Locate every blood parasite and identify its species.
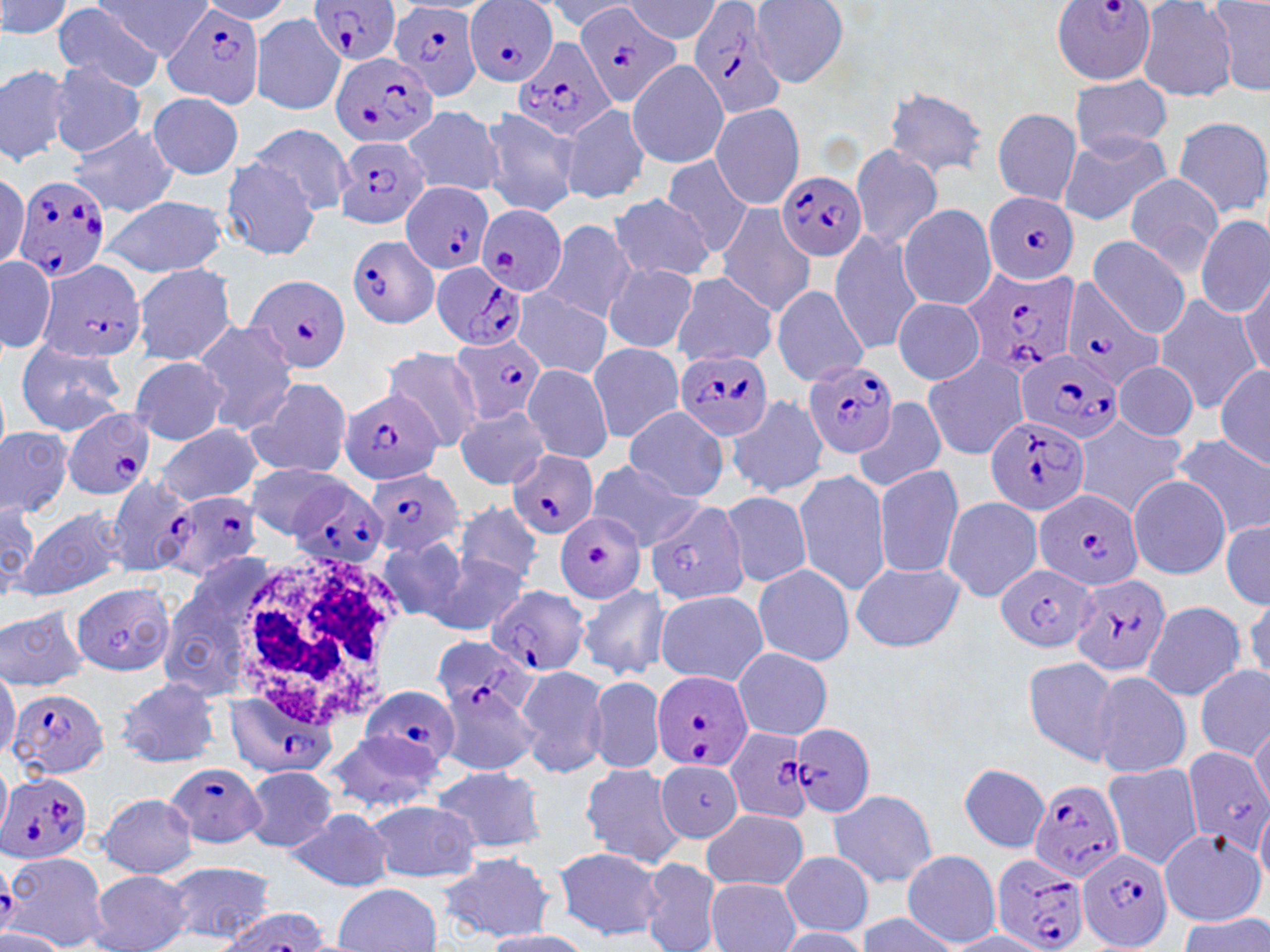
Approximate bounding boxes as named x1/y1/x2/y2 corners in pixels.
Plasmodium falciparum-infected red blood cells (subset): (x1=311, y1=0, x2=402, y2=67), (x1=573, y1=1, x2=683, y2=109), (x1=686, y1=1, x2=788, y2=119), (x1=387, y1=2, x2=485, y2=102), (x1=464, y1=2, x2=560, y2=86), (x1=1051, y1=2, x2=1158, y2=87), (x1=163, y1=4, x2=267, y2=108), (x1=513, y1=36, x2=618, y2=140), (x1=330, y1=50, x2=440, y2=148), (x1=336, y1=135, x2=431, y2=231), (x1=776, y1=171, x2=866, y2=263), (x1=13, y1=175, x2=111, y2=285), (x1=402, y1=181, x2=496, y2=276), (x1=983, y1=191, x2=1079, y2=285), (x1=475, y1=204, x2=567, y2=296), (x1=347, y1=235, x2=439, y2=328), (x1=34, y1=259, x2=147, y2=366), (x1=431, y1=262, x2=530, y2=351), (x1=963, y1=268, x2=1080, y2=379), (x1=243, y1=273, x2=349, y2=375), (x1=1058, y1=280, x2=1165, y2=390), (x1=453, y1=330, x2=546, y2=426), (x1=1015, y1=346, x2=1124, y2=447), (x1=675, y1=347, x2=773, y2=442), (x1=803, y1=358, x2=898, y2=459), (x1=339, y1=385, x2=443, y2=488), (x1=64, y1=408, x2=155, y2=499), (x1=983, y1=414, x2=1091, y2=517), (x1=509, y1=451, x2=597, y2=540), (x1=366, y1=467, x2=468, y2=559), (x1=104, y1=474, x2=193, y2=578), (x1=285, y1=481, x2=389, y2=571), (x1=1033, y1=487, x2=1143, y2=594), (x1=158, y1=492, x2=263, y2=583), (x1=641, y1=500, x2=749, y2=605), (x1=553, y1=514, x2=646, y2=605), (x1=995, y1=563, x2=1098, y2=654), (x1=1070, y1=573, x2=1172, y2=679), (x1=68, y1=581, x2=175, y2=677), (x1=485, y1=586, x2=590, y2=678), (x1=431, y1=638, x2=537, y2=721), (x1=651, y1=669, x2=753, y2=773), (x1=361, y1=686, x2=458, y2=770), (x1=225, y1=688, x2=337, y2=780), (x1=7, y1=689, x2=106, y2=780), (x1=790, y1=724, x2=876, y2=818), (x1=723, y1=727, x2=815, y2=823), (x1=1180, y1=747, x2=1270, y2=854), (x1=166, y1=762, x2=266, y2=848), (x1=0, y1=773, x2=94, y2=866), (x1=1029, y1=780, x2=1127, y2=884), (x1=1077, y1=845, x2=1173, y2=951), (x1=992, y1=850, x2=1090, y2=952).
No Plasmodium ovale, Plasmodium malariae, Plasmodium vivax, Babesia divergens, or Trypanosoma brucei observed.

slide-level diagnosis = Plasmodium falciparum
field of view = one of a larger specimen
modality = light microscopy
white blood cell locations = approximate bounding boxes as named x1/y1/x2/y2 corners in pixels: (x1=234, y1=548, x2=408, y2=725)
image size = 1270×952 pixels
stain = May-Grünwald-Giemsa
magnification = 1000x
preparation = thin blood film
uninfected red blood cell locations (subset) = approximate bounding boxes as named x1/y1/x2/y2 corners in pixels: (x1=0, y1=0, x2=74, y2=43), (x1=99, y1=0, x2=212, y2=59), (x1=197, y1=0, x2=295, y2=23), (x1=1209, y1=0, x2=1270, y2=98), (x1=542, y1=1, x2=638, y2=33), (x1=623, y1=1, x2=722, y2=43), (x1=748, y1=1, x2=851, y2=88), (x1=1136, y1=1, x2=1239, y2=102), (x1=53, y1=4, x2=166, y2=89), (x1=250, y1=13, x2=345, y2=116), (x1=627, y1=60, x2=730, y2=169), (x1=0, y1=62, x2=74, y2=167), (x1=47, y1=62, x2=147, y2=156), (x1=1069, y1=74, x2=1171, y2=156), (x1=883, y1=86, x2=990, y2=178), (x1=146, y1=92, x2=244, y2=180), (x1=709, y1=103, x2=804, y2=208), (x1=559, y1=104, x2=651, y2=204), (x1=477, y1=106, x2=579, y2=218), (x1=402, y1=107, x2=505, y2=198), (x1=992, y1=109, x2=1081, y2=205), (x1=1173, y1=115, x2=1270, y2=220), (x1=243, y1=122, x2=356, y2=215), (x1=66, y1=124, x2=175, y2=217), (x1=1057, y1=130, x2=1171, y2=227), (x1=850, y1=146, x2=945, y2=251), (x1=662, y1=156, x2=754, y2=259), (x1=219, y1=160, x2=323, y2=260), (x1=0, y1=172, x2=29, y2=271), (x1=1122, y1=174, x2=1223, y2=276), (x1=609, y1=192, x2=715, y2=283), (x1=100, y1=194, x2=228, y2=278), (x1=717, y1=204, x2=816, y2=318), (x1=897, y1=204, x2=997, y2=311), (x1=1196, y1=215, x2=1268, y2=318), (x1=539, y1=219, x2=639, y2=324), (x1=828, y1=230, x2=922, y2=354), (x1=743, y1=234, x2=838, y2=366), (x1=1086, y1=235, x2=1190, y2=337), (x1=0, y1=255, x2=56, y2=354), (x1=602, y1=263, x2=699, y2=354), (x1=131, y1=264, x2=237, y2=366), (x1=672, y1=273, x2=777, y2=370), (x1=1236, y1=275, x2=1269, y2=381), (x1=772, y1=284, x2=869, y2=387), (x1=513, y1=293, x2=611, y2=380), (x1=1153, y1=296, x2=1259, y2=415), (x1=892, y1=298, x2=985, y2=383), (x1=191, y1=320, x2=298, y2=434), (x1=13, y1=340, x2=128, y2=435), (x1=587, y1=343, x2=685, y2=441), (x1=380, y1=347, x2=485, y2=449), (x1=922, y1=353, x2=1028, y2=460), (x1=129, y1=357, x2=229, y2=445), (x1=1113, y1=360, x2=1198, y2=442), (x1=1215, y1=363, x2=1270, y2=470), (x1=521, y1=364, x2=612, y2=464), (x1=245, y1=376, x2=352, y2=479), (x1=726, y1=394, x2=828, y2=499), (x1=853, y1=398, x2=945, y2=495), (x1=621, y1=405, x2=731, y2=503), (x1=453, y1=406, x2=550, y2=489), (x1=1073, y1=418, x2=1186, y2=517), (x1=154, y1=423, x2=262, y2=506), (x1=0, y1=426, x2=72, y2=520), (x1=1171, y1=433, x2=1270, y2=538), (x1=585, y1=460, x2=702, y2=549), (x1=872, y1=463, x2=964, y2=578), (x1=793, y1=470, x2=891, y2=593), (x1=1128, y1=476, x2=1231, y2=579), (x1=720, y1=491, x2=812, y2=588), (x1=941, y1=496, x2=1044, y2=603), (x1=0, y1=501, x2=38, y2=600), (x1=454, y1=503, x2=543, y2=588), (x1=16, y1=506, x2=126, y2=603), (x1=1220, y1=517, x2=1270, y2=608), (x1=376, y1=536, x2=473, y2=627), (x1=431, y1=552, x2=528, y2=638), (x1=850, y1=561, x2=964, y2=653), (x1=158, y1=563, x2=276, y2=699), (x1=751, y1=563, x2=856, y2=666), (x1=577, y1=583, x2=669, y2=679), (x1=654, y1=589, x2=768, y2=686), (x1=1244, y1=592, x2=1270, y2=688), (x1=1142, y1=600, x2=1245, y2=701), (x1=0, y1=605, x2=92, y2=692), (x1=732, y1=647, x2=833, y2=739), (x1=1022, y1=656, x2=1120, y2=765), (x1=0, y1=664, x2=19, y2=762), (x1=512, y1=664, x2=609, y2=778), (x1=1195, y1=665, x2=1269, y2=761), (x1=1086, y1=668, x2=1191, y2=778), (x1=587, y1=675, x2=666, y2=774), (x1=115, y1=676, x2=222, y2=768), (x1=1247, y1=718, x2=1270, y2=814), (x1=319, y1=731, x2=445, y2=815), (x1=581, y1=761, x2=684, y2=868), (x1=1104, y1=761, x2=1205, y2=872), (x1=0, y1=762, x2=11, y2=838), (x1=958, y1=763, x2=1050, y2=852), (x1=431, y1=765, x2=546, y2=855), (x1=241, y1=766, x2=340, y2=853), (x1=829, y1=788, x2=937, y2=888), (x1=97, y1=793, x2=200, y2=878), (x1=366, y1=801, x2=481, y2=883), (x1=1254, y1=802, x2=1270, y2=888), (x1=700, y1=806, x2=809, y2=893), (x1=287, y1=807, x2=394, y2=890), (x1=1157, y1=828, x2=1265, y2=927), (x1=552, y1=847, x2=666, y2=940), (x1=12, y1=850, x2=111, y2=950), (x1=902, y1=850, x2=1002, y2=948), (x1=779, y1=851, x2=875, y2=937), (x1=436, y1=852, x2=556, y2=943), (x1=638, y1=858, x2=724, y2=952), (x1=160, y1=860, x2=276, y2=945), (x1=89, y1=869, x2=195, y2=952), (x1=706, y1=877, x2=799, y2=952), (x1=330, y1=883, x2=443, y2=952), (x1=855, y1=912, x2=962, y2=951), (x1=1177, y1=913, x2=1270, y2=952), (x1=0, y1=927, x2=66, y2=951), (x1=771, y1=927, x2=871, y2=950), (x1=477, y1=930, x2=600, y2=952), (x1=943, y1=931, x2=1051, y2=951)